Classify this cell by malaria status.
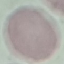
It is uninfected.

Summary:
  - Capture: smartphone camera at the microscope eyepiece
  - Stain: Giemsa
  - Preparation: thin blood smear
  - Image type: automatically extracted cell patch, resized to 64 × 64 pixels